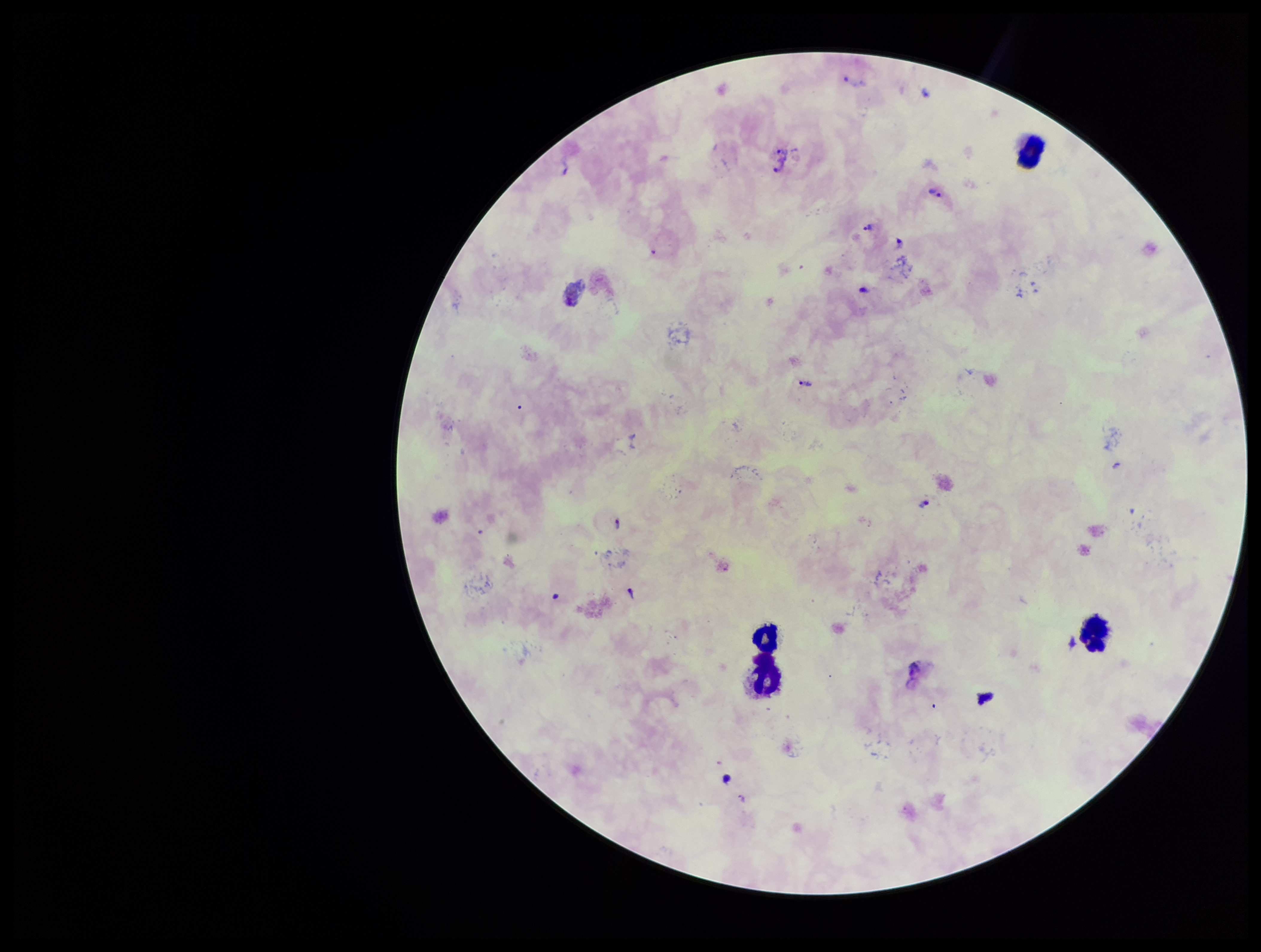
patient malaria status = infected
species reported for this patient = Plasmodium vivax
stain = Giemsa
parasite count = 16
field of view = single
Plasmodium parasites = seen
preparation = thick blood smear
leukocyte count = 4
capture = smartphone photograph through the microscope eyepiece
image size = 1261×952 pixels